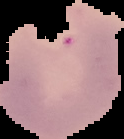

image size = 124×139 pixels
preparation = thin blood smear
malaria status = parasitized
image type = segmented cell region with the area outside set to black